Give the position of every malaria parasite.
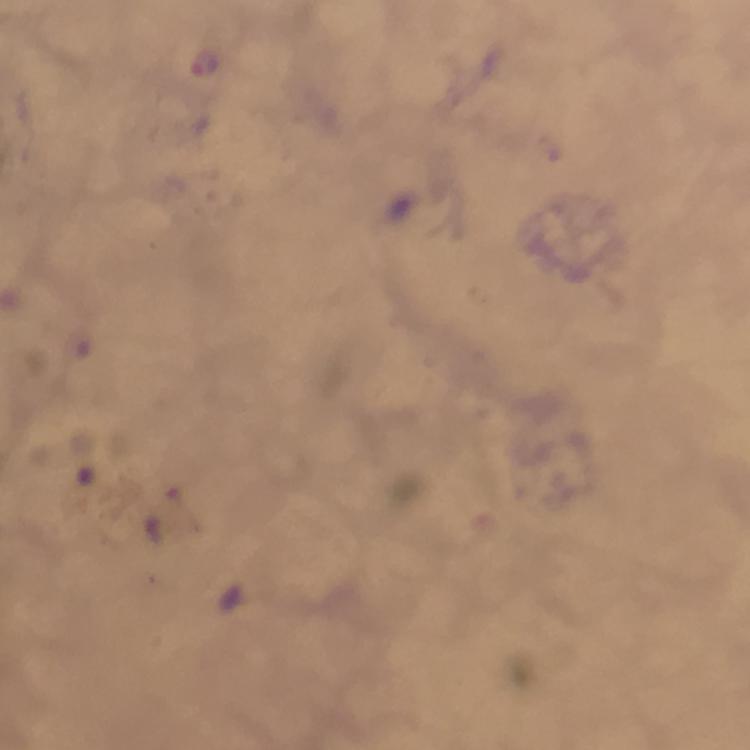

Approximate object centers, in pixels from the top-left corner.
Malaria parasites: (x=206, y=63).

From a diagnostic examination for malaria. Immersion oil applied. 100x magnification. Image is 750×750 pixels. Cropped region of a single field of view. Photographed through the microscope with a smartphone camera. Thick blood film. Giemsa stain.